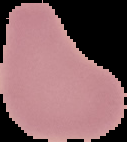
malaria_status: uninfected
image_size: 127×142 pixels
preparation: thin blood film
image_type: segmented cell region with the area outside set to black